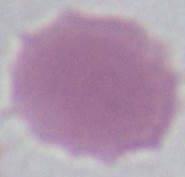
Summary:
  - Modality: micrograph
  - Identification: erythrocyte
  - Magnification: 1000x